State the blood parasite species.
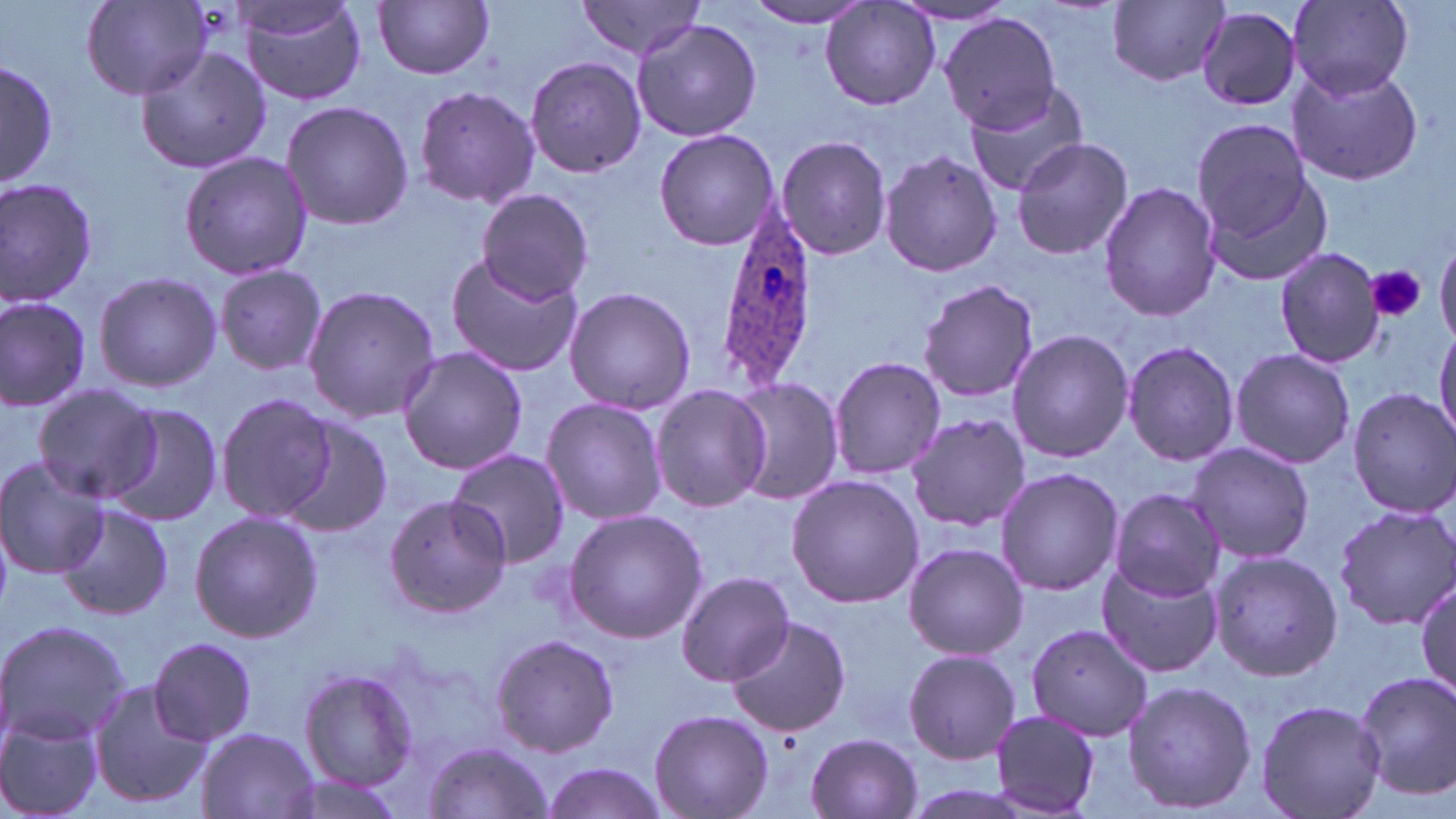

Plasmodium ovale.

Summary:
  - Coordinate format: approximate bounding boxes as (x1, y1, x2, y2) in pixels
  - Plasmodium ovale-infected red blood cell locations: (710, 203, 819, 391)
  - Uninfected red blood cell locations: (241, 0, 367, 105), (577, 0, 707, 59), (80, 1, 213, 100), (372, 1, 496, 80), (742, 1, 882, 27), (1109, 1, 1227, 86), (1288, 1, 1414, 98), (819, 2, 940, 111), (895, 2, 1020, 26), (1197, 7, 1302, 112), (939, 12, 1066, 136), (632, 20, 764, 141), (134, 46, 271, 174), (524, 57, 648, 178), (0, 60, 55, 193), (1285, 64, 1427, 187), (965, 83, 1094, 199), (413, 85, 541, 210), (281, 99, 413, 231), (1189, 116, 1315, 239), (653, 128, 779, 251), (776, 134, 891, 261), (1010, 135, 1134, 262), (878, 149, 1002, 278), (178, 150, 313, 280), (1200, 169, 1335, 289), (0, 177, 99, 308), (1098, 180, 1222, 322), (476, 188, 593, 305), (1436, 237, 1456, 347), (1274, 246, 1385, 369), (444, 253, 582, 378), (213, 267, 331, 375), (93, 272, 222, 391), (916, 277, 1041, 405), (303, 285, 441, 423), (562, 286, 697, 415), (0, 294, 94, 409), (1433, 325, 1456, 444), (1007, 328, 1134, 464), (1120, 339, 1242, 468), (398, 346, 527, 474), (1229, 348, 1356, 468), (829, 355, 947, 481), (726, 378, 843, 506), (32, 383, 158, 503), (650, 384, 770, 513), (1348, 388, 1456, 517), (214, 392, 340, 525), (540, 396, 666, 527), (102, 401, 223, 527), (904, 413, 1030, 533), (278, 418, 395, 538), (1186, 442, 1316, 567), (447, 447, 570, 568), (0, 458, 112, 578), (994, 467, 1124, 596), (785, 473, 923, 609), (1108, 487, 1225, 601), (382, 496, 512, 617), (60, 502, 175, 619), (1331, 503, 1456, 630), (563, 508, 707, 645), (190, 511, 324, 644), (901, 541, 1028, 660), (1207, 549, 1343, 683), (1095, 556, 1222, 678), (676, 572, 795, 687), (1415, 574, 1456, 702), (727, 615, 851, 736), (0, 620, 129, 744), (1025, 621, 1154, 743), (489, 633, 621, 757), (147, 636, 257, 746), (902, 648, 1022, 765), (298, 669, 418, 788), (1352, 670, 1456, 797), (86, 679, 211, 812), (1122, 679, 1257, 813), (1255, 698, 1387, 819), (648, 709, 773, 818), (989, 709, 1101, 815), (0, 712, 105, 819), (196, 725, 320, 818), (807, 733, 922, 818), (424, 741, 552, 817), (539, 760, 669, 819), (277, 772, 407, 818)
  - Platelet locations: (1369, 264, 1425, 323)
  - Stain: May-Grünwald-Giemsa
  - Modality: light microscopy
  - Image size: 1456×819 pixels
  - Magnification: 1000x
  - Preparation: thin blood smear
  - Field of view: one of a larger specimen